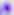

{
  "identification": "Toxoplasma gondii",
  "modality": "micrograph",
  "magnification": "400x"
}